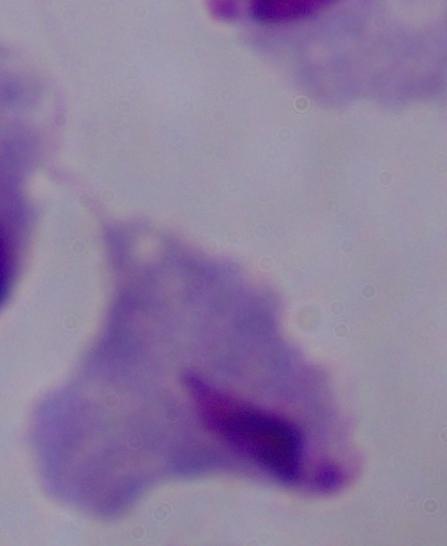
magnification = 1000x
identification = trichomonad
modality = photomicrograph